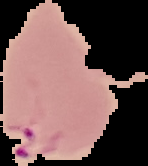
Malaria status: parasitized. Image is 148×166 pixels. From a thin blood smear. Segmented cell region on a black background.